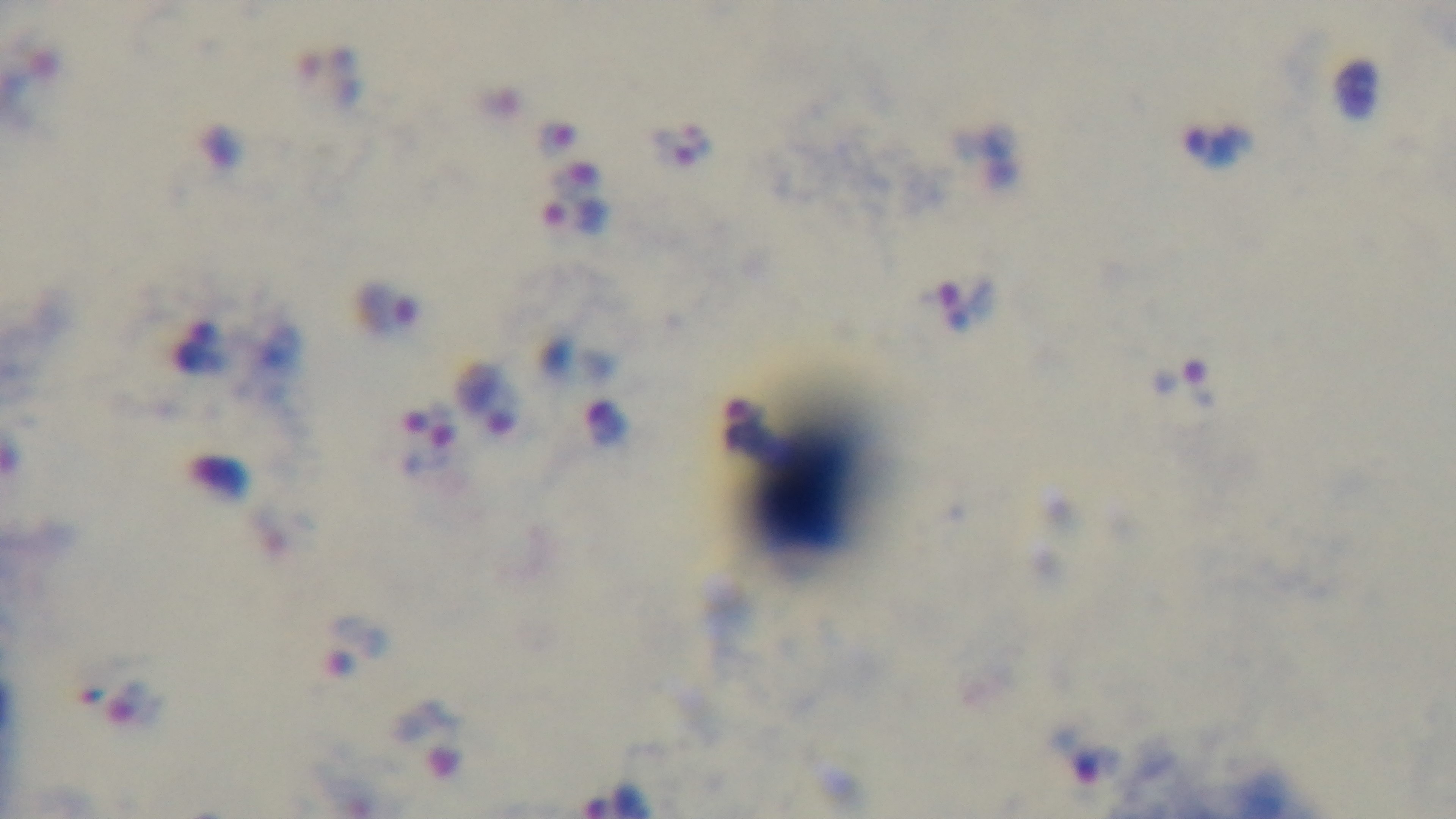

field_of_view: single
modality: light microscopy
capture: mounted 4K digital camera
malaria_status: infected
preparation: thick
stain: Giemsa
objective: 100x oil immersion